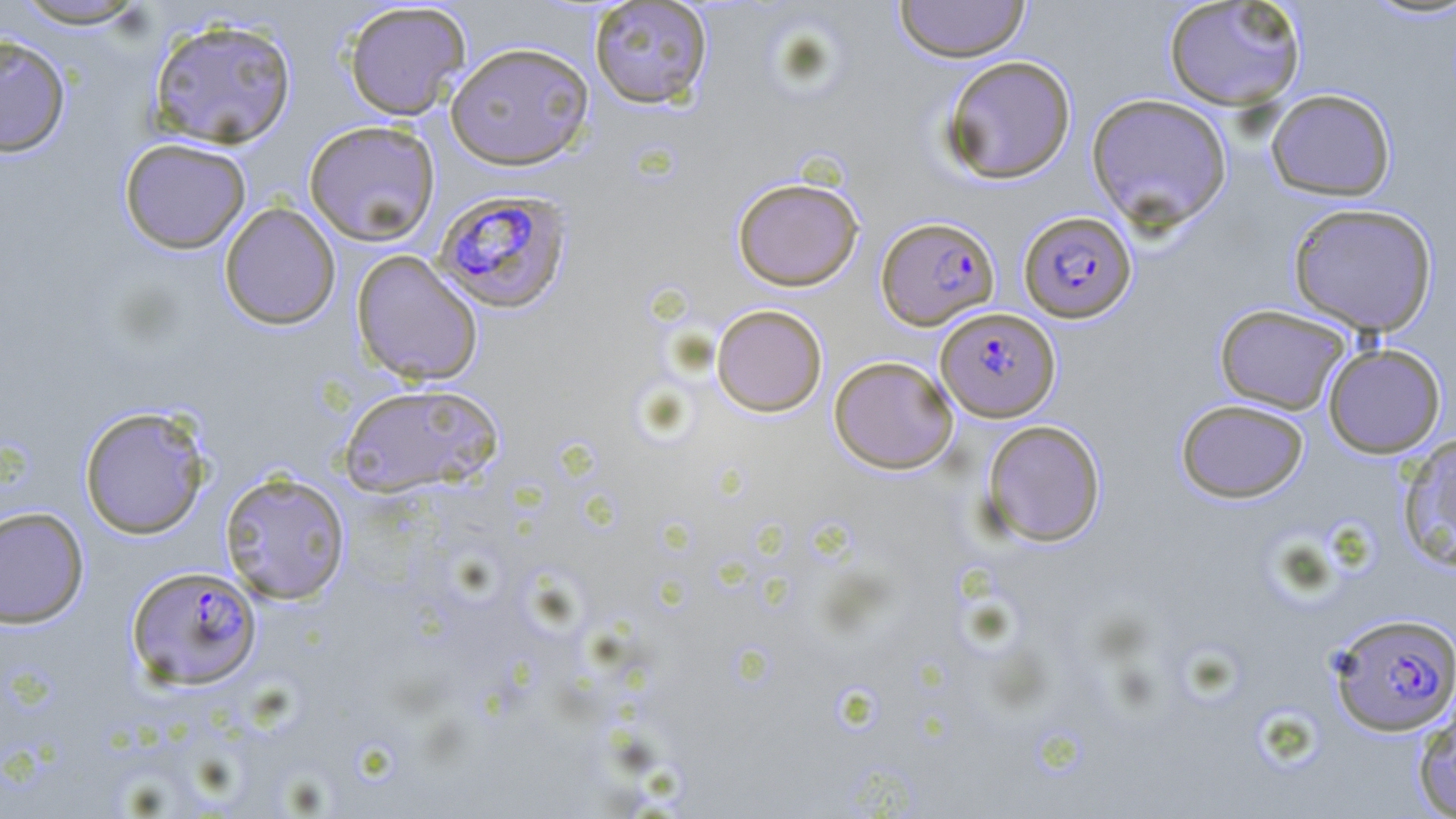

slide-level diagnosis = Plasmodium falciparum
field of view = one of a larger specimen
uninfected red blood cell locations = approximate bounding boxes as (x1,y1)-(x2,y2) corner pairs in pixels: (894,0)-(1030,62), (1163,0)-(1307,110), (8,1)-(153,29), (588,1)-(713,109), (342,2)-(471,121), (148,17)-(297,149), (0,33)-(71,158), (445,41)-(595,170), (940,55)-(1077,185), (1266,88)-(1396,201), (1086,92)-(1232,230), (303,120)-(441,246), (118,137)-(251,254), (732,177)-(864,291), (219,202)-(341,330), (1288,202)-(1438,337), (351,249)-(484,386), (711,304)-(827,417), (1214,304)-(1352,415), (1322,343)-(1446,458), (828,355)-(958,474), (337,382)-(503,498), (1176,399)-(1309,503), (78,405)-(211,540), (981,419)-(1106,547), (1398,433)-(1456,572), (219,470)-(351,605), (0,506)-(90,629), (1412,694)-(1456,818)
modality = optical microscopy
stain = May-Grünwald-Giemsa
Plasmodium falciparum-infected red blood cell locations = approximate bounding boxes as (x1,y1)-(x2,y2) corner pairs in pixels: (432,188)-(573,314), (1018,211)-(1137,323), (876,216)-(1000,329), (936,307)-(1060,421), (127,565)-(262,690), (1327,612)-(1456,736)
magnification = 1000x
image size = 1456×819 pixels
preparation = thin blood smear